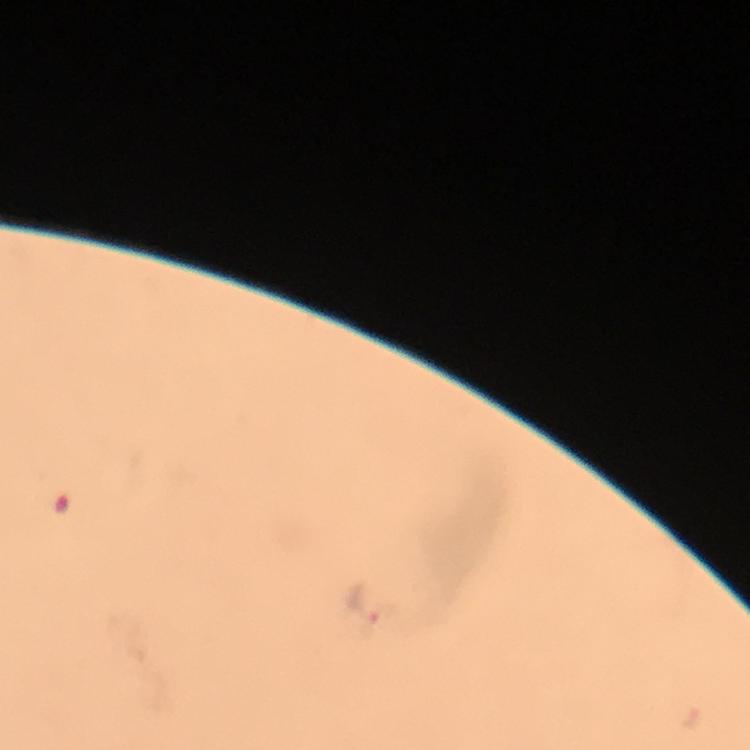

cropped_from: one field of view
immersion_oil: used
stain: Giemsa
capture: smartphone camera through the microscope
image_size: 750×750 pixels
malaria_parasite_locations: 'approximate object centers, in pixels from the top-left corner: (x=362, y=602)'
magnification: 100x
context: from a diagnostic examination for malaria
preparation: thick blood film